Locate and identify every blood parasite.
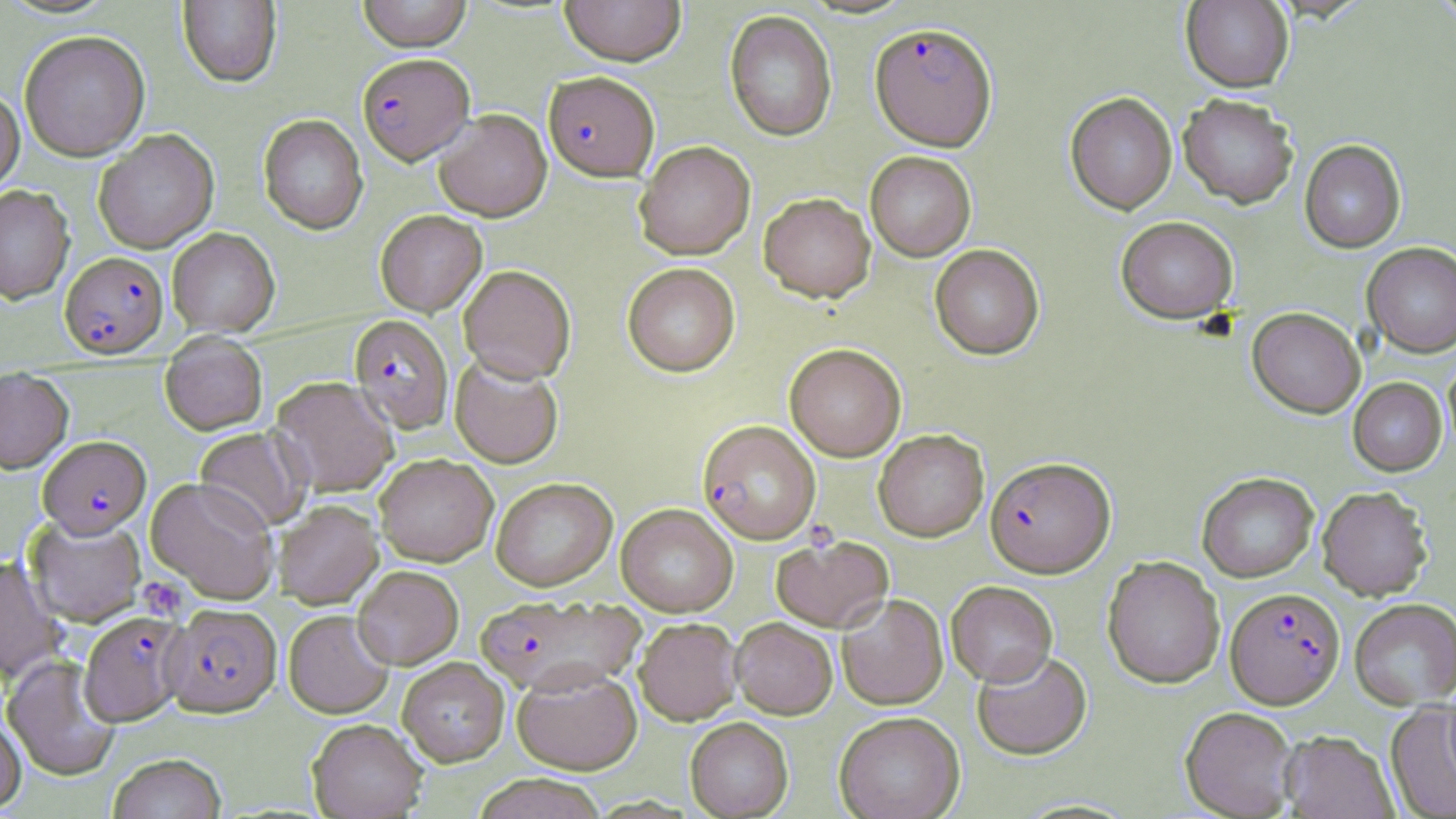
Approximate bounding boxes as (x1, y1, x2, y2) in pixels.
Plasmodium falciparum-infected red blood cells: (870, 23, 997, 151), (358, 53, 474, 164), (543, 72, 659, 181), (60, 251, 168, 358), (349, 315, 454, 433), (697, 419, 821, 544), (38, 435, 150, 537), (985, 456, 1115, 577), (1226, 587, 1345, 708), (474, 594, 644, 695), (163, 603, 282, 716), (79, 611, 188, 726).
No Plasmodium ovale, Plasmodium malariae, Plasmodium vivax, Babesia divergens, or Trypanosoma brucei observed.

Uninfected red blood cell locations: (357, 0, 472, 52), (559, 0, 686, 66), (177, 1, 282, 87), (1181, 1, 1294, 92), (724, 11, 838, 142), (19, 30, 150, 161), (0, 86, 24, 194), (1065, 92, 1177, 214), (1178, 94, 1299, 208), (433, 109, 552, 221), (258, 113, 368, 234), (94, 129, 219, 253), (1299, 139, 1406, 253), (635, 141, 755, 259), (865, 151, 976, 261), (0, 185, 74, 304), (759, 192, 876, 303), (375, 210, 487, 316), (1116, 215, 1238, 323), (167, 227, 280, 336), (1362, 242, 1456, 358), (930, 244, 1044, 360), (623, 263, 740, 377), (458, 264, 576, 382), (1247, 307, 1365, 418), (159, 337, 268, 436), (784, 343, 907, 461), (1444, 352, 1456, 458), (450, 354, 564, 468), (0, 367, 73, 473), (270, 376, 398, 497), (1348, 377, 1446, 476), (195, 427, 311, 532), (873, 429, 989, 541), (374, 454, 498, 566), (1197, 472, 1318, 584), (146, 477, 280, 604), (491, 477, 617, 591), (1317, 486, 1432, 600), (272, 499, 383, 608), (616, 503, 737, 616), (24, 515, 147, 627), (771, 534, 894, 632), (1102, 556, 1225, 689), (0, 557, 64, 686), (352, 565, 463, 669), (946, 581, 1058, 686), (836, 593, 948, 709), (1349, 598, 1456, 708), (283, 610, 394, 718), (634, 617, 742, 725), (731, 617, 837, 719), (972, 648, 1093, 760), (2, 655, 121, 781), (397, 658, 509, 766), (512, 666, 642, 775), (1385, 703, 1456, 818), (1180, 706, 1299, 818), (834, 711, 965, 819), (0, 715, 26, 813), (685, 717, 793, 818), (307, 718, 428, 818), (1280, 730, 1398, 818), (107, 753, 227, 818), (473, 773, 607, 819). Platelet locations: (137, 577, 187, 620). Slide-level diagnosis: Plasmodium falciparum. Image is 1456×819 pixels. Light microscopy. Thin blood smear. Captured at 1000x magnification. Single field of view. May-Grünwald-Giemsa stain.